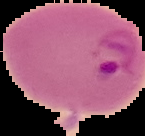

preparation = thin blood smear
image type = segmented cell region on a black background
result = malaria parasites identified
image size = 145×136 pixels